Locate every Plasmodium parasite.
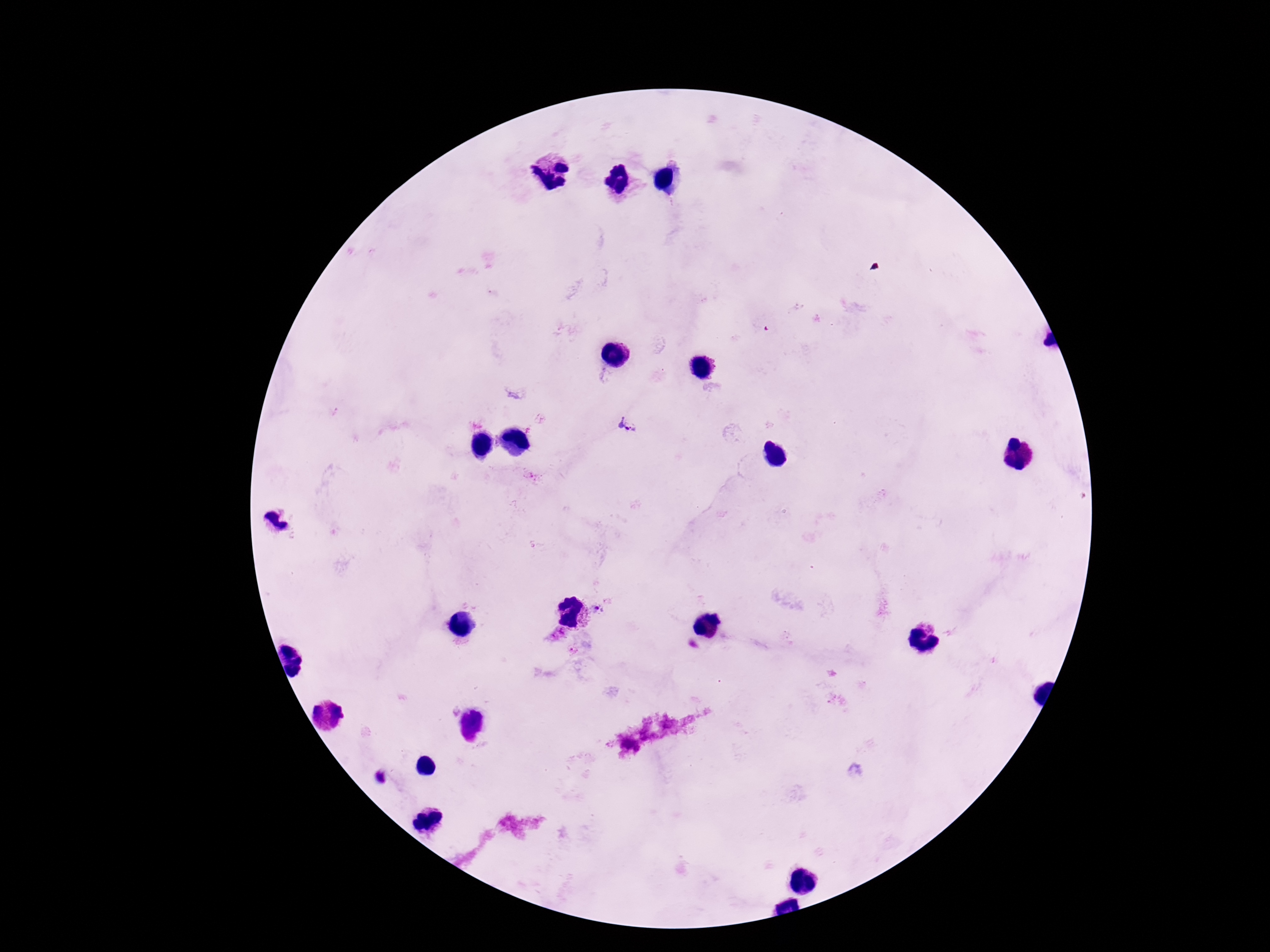

Approximate centers as {x, y} in pixels.
Plasmodium parasites: {628, 426}, {598, 611}, {555, 634}, {574, 651}.

Summary:
  - Preparation: thick peripheral-blood smear
  - Image size: 1270×952 pixels
  - Capture: smartphone camera through the microscope eyepiece
  - Patient malaria status: infected
  - Stain: Giemsa
  - Field of view: one from this slide
  - Magnification: 100x